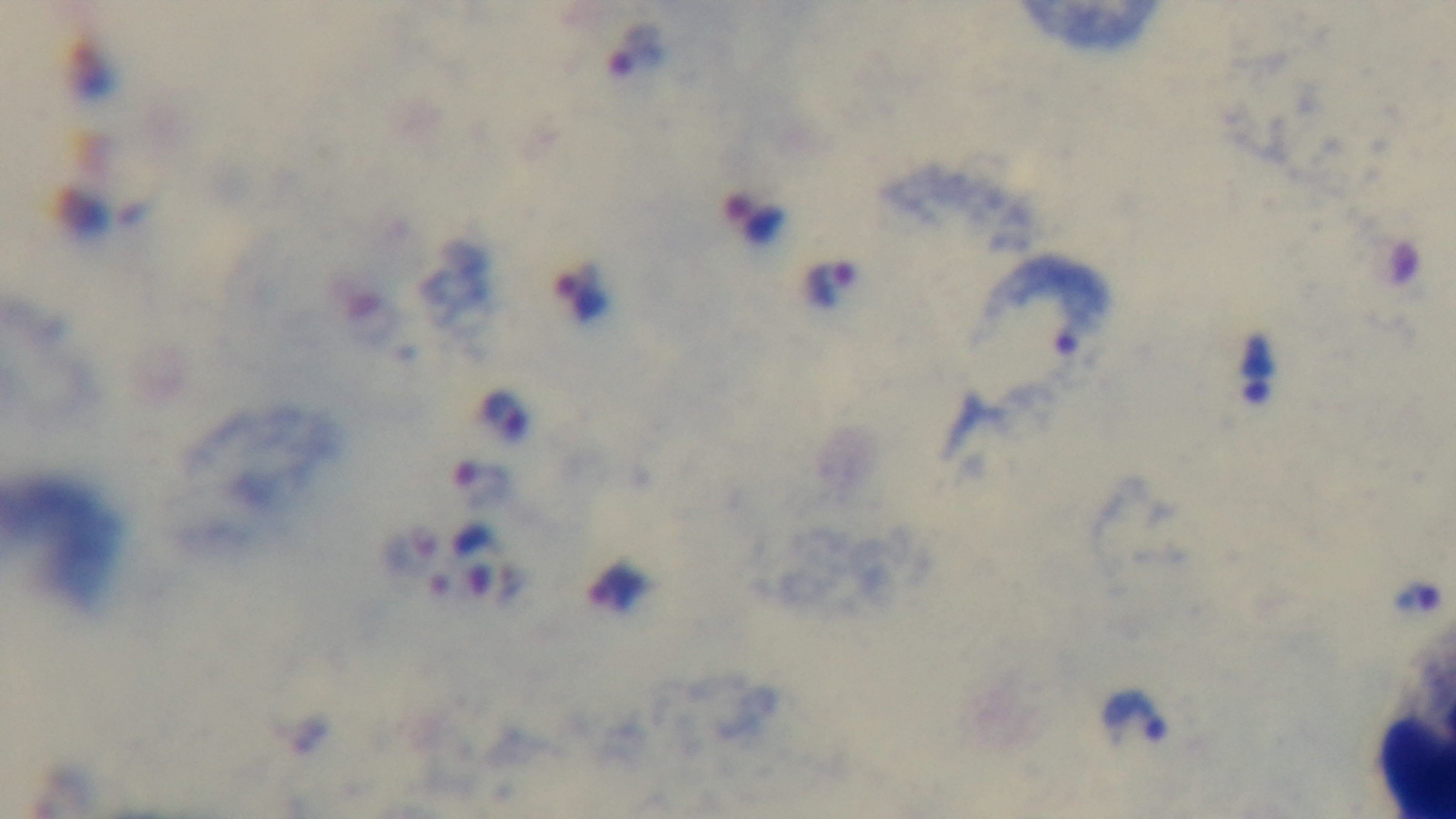

{
  "capture": "mounted 4K digital camera",
  "field_of_view": "one from the slide",
  "objective": "100x oil immersion",
  "stain": "Giemsa",
  "preparation": "thick",
  "malaria_status": "infected",
  "modality": "light microscopy"
}